Identify the parasite.
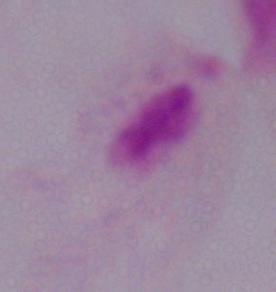

This is a trichomonad.

modality = photomicrograph
magnification = 1000x